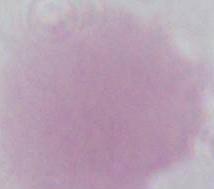

Summary:
  - Magnification: 1000x
  - Identification: red blood cell
  - Modality: micrograph